Assess the morphology of the red blood cells.
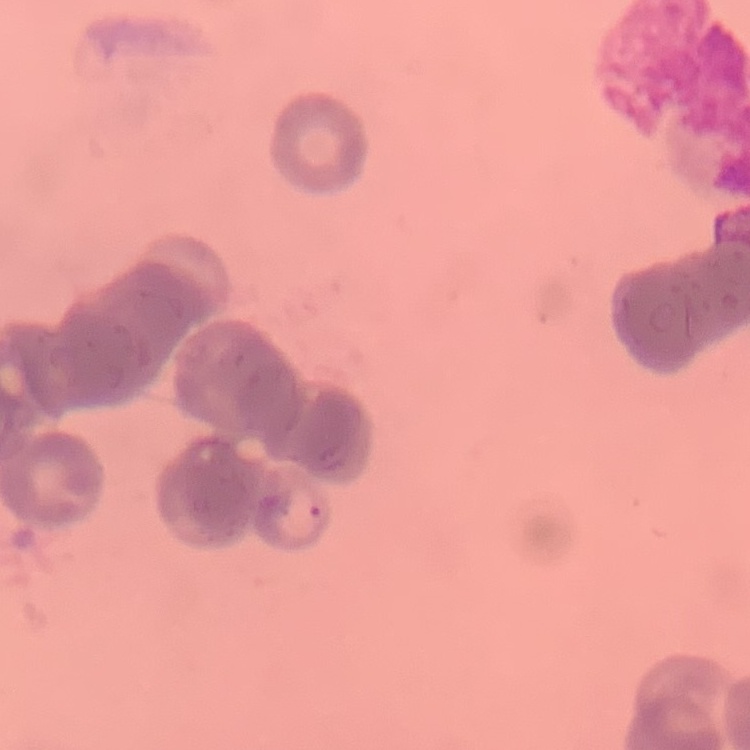
Rouleaux formation.

stain = Field's or Giemsa
image type = square crop of a larger photomicrograph
preparation = thin peripheral smear